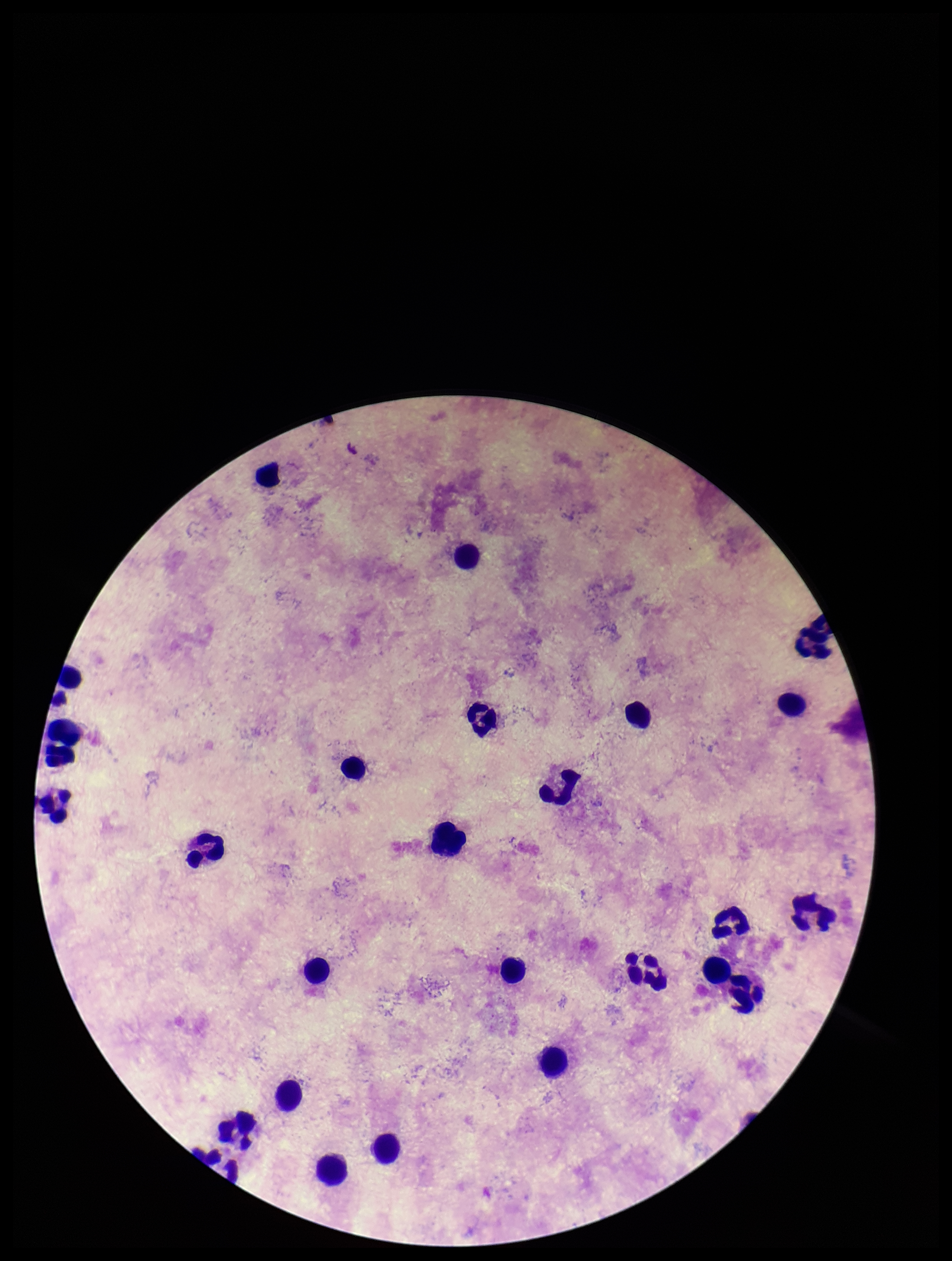
Summary:
  - Plasmodium parasites: none detected
  - Leukocyte count: 26
  - Field of view: one from this slide
  - Capture: smartphone photograph through the microscope eyepiece
  - Patient malaria status: negative
  - Image size: 952×1261 pixels
  - Preparation: thick smear
  - Parasite count: 0
  - Stain: Giemsa